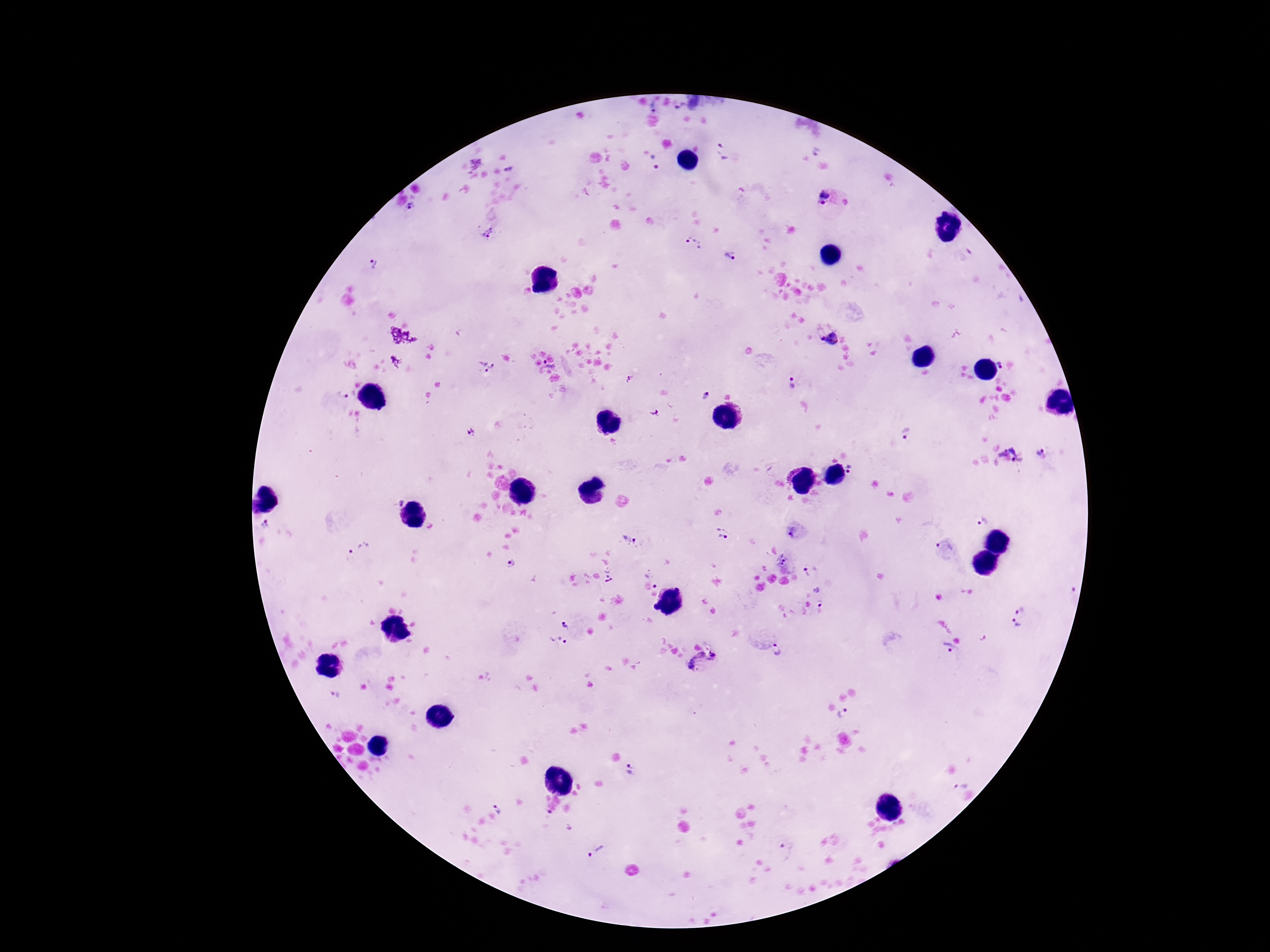
stain = Giemsa
magnification = 100x
Plasmodium parasite locations = approximate centers as (x, y) in pixels: (724, 151), (815, 152), (655, 160), (510, 169), (824, 193), (823, 203), (412, 207), (486, 232), (694, 244), (729, 256), (373, 264), (829, 339), (1001, 364), (550, 366), (485, 368), (629, 379), (792, 383), (705, 395), (655, 413), (472, 432), (906, 434), (1042, 453), (1009, 455), (852, 469), (400, 502), (982, 521), (266, 524), (793, 532), (723, 534), (629, 540), (945, 550), (361, 551), (784, 558), (510, 565), (811, 572), (609, 575), (656, 585), (1070, 589), (824, 598), (1019, 608), (565, 625), (1016, 626), (558, 642), (778, 649), (949, 651), (707, 667), (336, 695), (844, 713), (630, 771), (960, 783), (499, 808), (548, 819), (598, 850), (787, 850)
field of view = single
capture = smartphone camera through the microscope eyepiece
patient malaria status = infected
image size = 1270×952 pixels
preparation = thick blood film